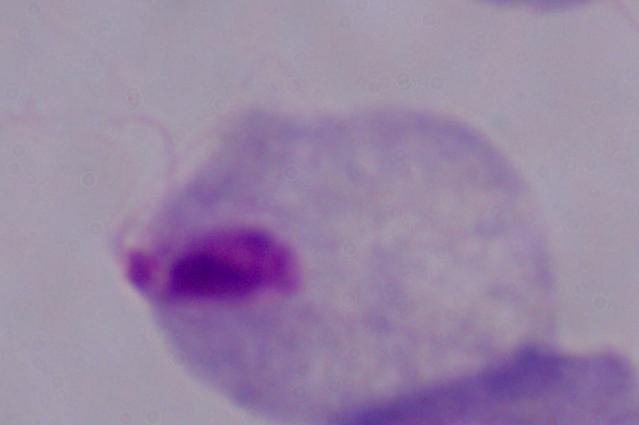 A trichomonad is shown. Micrograph. 1000x magnification.